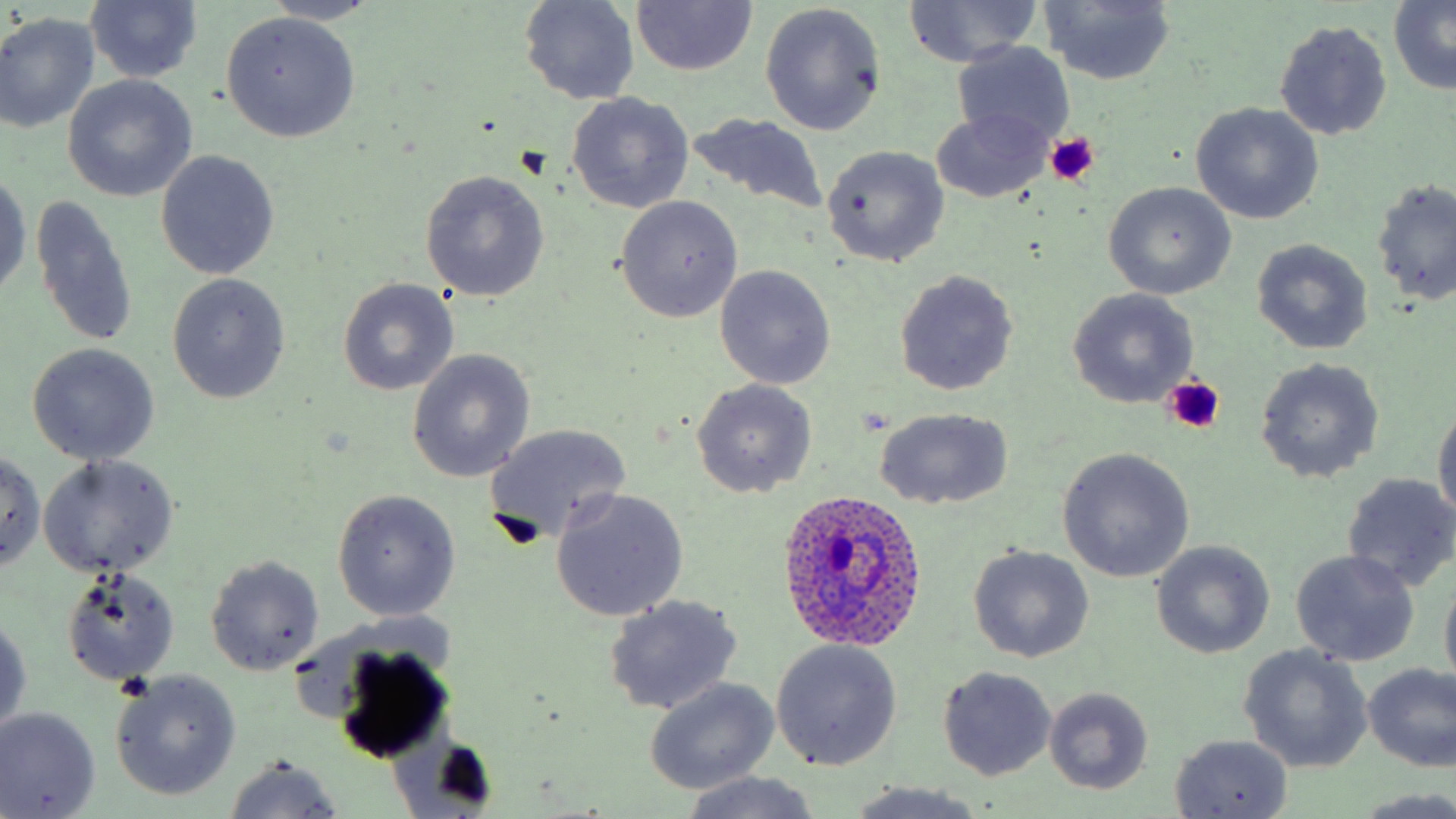

slide_level_diagnosis: Plasmodium ovale
preparation: thin blood film
magnification: 1000x
stain: May-Grünwald-Giemsa
platelet_locations: 'approximate bounding boxes as named x1/y1/x2/y2 corners in pixels: (x1=1044, y1=132, x2=1100, y2=185), (x1=1160, y1=378, x2=1224, y2=432)'
plasmodium_ovale_infected_red_blood_cell_locations: 'approximate bounding boxes as named x1/y1/x2/y2 corners in pixels: (x1=776, y1=488, x2=929, y2=651)'
uninfected_red_blood_cell_locations: 'approximate bounding boxes as named x1/y1/x2/y2 corners in pixels: (x1=264, y1=0, x2=384, y2=26), (x1=518, y1=0, x2=639, y2=106), (x1=902, y1=0, x2=1041, y2=67), (x1=631, y1=1, x2=756, y2=75), (x1=1037, y1=1, x2=1177, y2=86), (x1=1387, y1=1, x2=1456, y2=93), (x1=84, y1=2, x2=203, y2=85), (x1=761, y1=4, x2=886, y2=137), (x1=220, y1=12, x2=361, y2=143), (x1=0, y1=14, x2=100, y2=134), (x1=1274, y1=19, x2=1392, y2=142), (x1=952, y1=42, x2=1076, y2=149), (x1=4, y1=44, x2=153, y2=181), (x1=63, y1=75, x2=196, y2=201), (x1=565, y1=92, x2=695, y2=215), (x1=1192, y1=103, x2=1323, y2=224), (x1=931, y1=108, x2=1052, y2=203), (x1=683, y1=113, x2=831, y2=218), (x1=821, y1=145, x2=950, y2=267), (x1=155, y1=151, x2=280, y2=280), (x1=419, y1=169, x2=549, y2=303), (x1=0, y1=172, x2=30, y2=299), (x1=1371, y1=179, x2=1456, y2=306), (x1=1104, y1=181, x2=1236, y2=299), (x1=614, y1=195, x2=743, y2=322), (x1=31, y1=196, x2=139, y2=348), (x1=1251, y1=238, x2=1372, y2=355), (x1=714, y1=265, x2=836, y2=390), (x1=892, y1=269, x2=1019, y2=397), (x1=165, y1=273, x2=291, y2=404), (x1=338, y1=277, x2=460, y2=395), (x1=1068, y1=289, x2=1198, y2=408), (x1=26, y1=343, x2=161, y2=465), (x1=407, y1=350, x2=534, y2=483), (x1=1254, y1=357, x2=1385, y2=484), (x1=690, y1=378, x2=817, y2=498), (x1=1431, y1=401, x2=1456, y2=524), (x1=873, y1=406, x2=1015, y2=511), (x1=482, y1=423, x2=632, y2=547), (x1=1056, y1=447, x2=1194, y2=582), (x1=0, y1=452, x2=47, y2=573), (x1=38, y1=454, x2=179, y2=578), (x1=1342, y1=472, x2=1456, y2=592), (x1=331, y1=488, x2=461, y2=622), (x1=550, y1=490, x2=689, y2=619), (x1=1150, y1=541, x2=1274, y2=658), (x1=967, y1=545, x2=1094, y2=662), (x1=1291, y1=549, x2=1421, y2=666), (x1=204, y1=555, x2=324, y2=675), (x1=59, y1=567, x2=180, y2=686), (x1=1439, y1=570, x2=1456, y2=692), (x1=602, y1=595, x2=743, y2=716), (x1=1, y1=613, x2=30, y2=736), (x1=772, y1=640, x2=902, y2=771), (x1=327, y1=641, x2=455, y2=762), (x1=1238, y1=645, x2=1372, y2=773), (x1=1361, y1=662, x2=1455, y2=770), (x1=937, y1=666, x2=1058, y2=781), (x1=110, y1=670, x2=242, y2=803), (x1=644, y1=677, x2=780, y2=794), (x1=1044, y1=687, x2=1153, y2=795), (x1=0, y1=707, x2=100, y2=818), (x1=1170, y1=734, x2=1293, y2=817), (x1=224, y1=756, x2=344, y2=818), (x1=678, y1=772, x2=822, y2=818), (x1=841, y1=782, x2=991, y2=819), (x1=1357, y1=790, x2=1456, y2=817)'
image_size: 1456×819 pixels
modality: light microscopy
field_of_view: one of a larger specimen